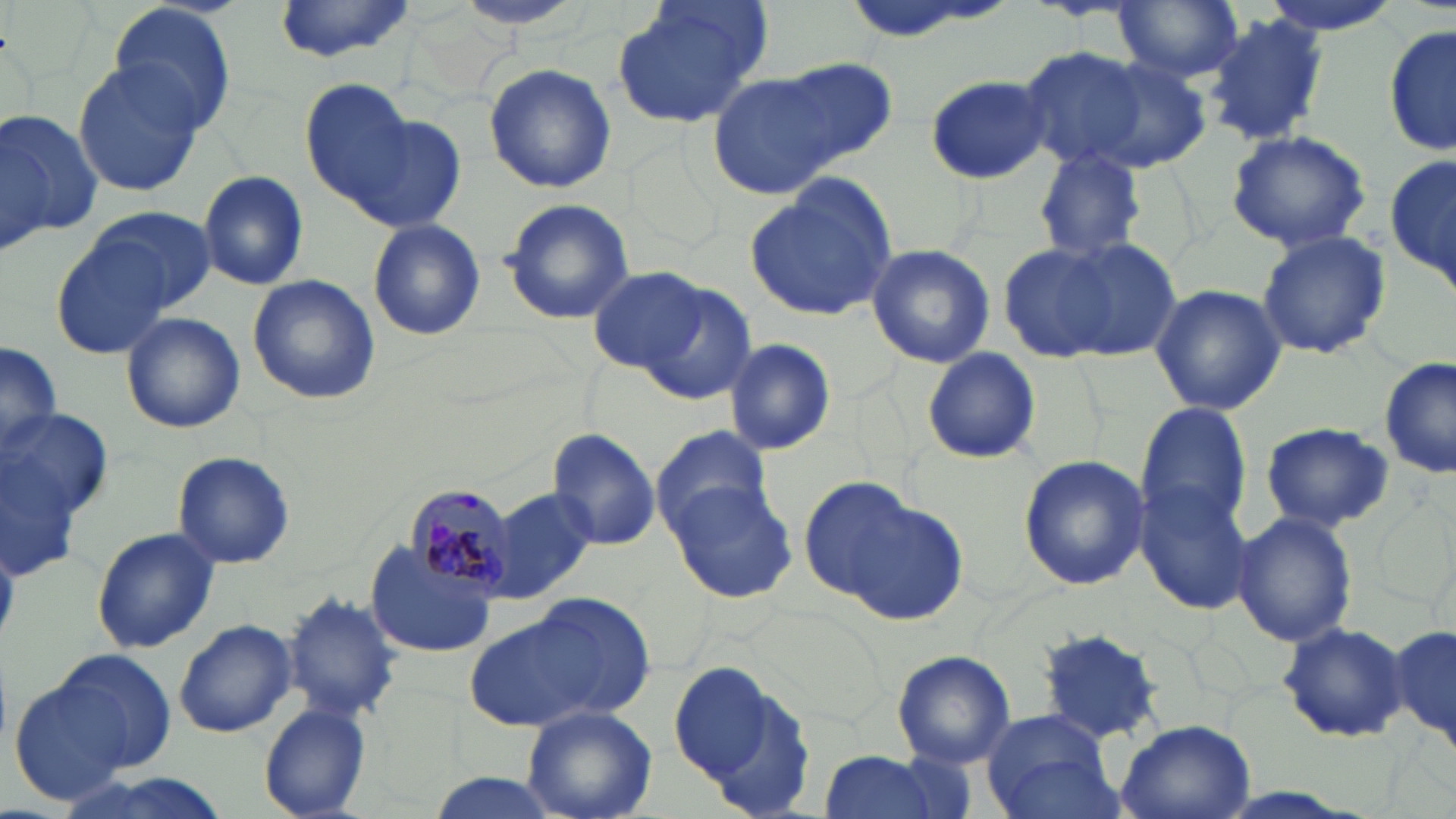

slide-level diagnosis = Plasmodium malariae
stain = May-Grünwald-Giemsa
modality = light microscopy
Plasmodium malariae-infected red blood cell locations = approximate bounding boxes as [x1, y1, x2, y2] in pixels: [400, 483, 522, 603]
preparation = thin blood film
uninfected red blood cell locations = approximate bounding boxes as [x1, y1, x2, y2] in pixels: [272, 0, 417, 62], [459, 0, 591, 30], [609, 0, 771, 130], [1112, 0, 1245, 83], [109, 3, 236, 131], [1203, 15, 1329, 144], [1385, 21, 1456, 162], [1020, 46, 1155, 171], [1063, 54, 1217, 176], [779, 58, 898, 163], [73, 62, 205, 197], [483, 63, 617, 193], [706, 70, 857, 202], [921, 72, 1051, 183], [300, 81, 420, 209], [0, 109, 100, 243], [343, 111, 466, 235], [1226, 129, 1372, 253], [1033, 149, 1151, 267], [1386, 152, 1455, 295], [198, 172, 310, 289], [745, 178, 897, 323], [500, 199, 635, 323], [91, 206, 215, 312], [367, 217, 486, 342], [1254, 230, 1392, 359], [50, 233, 175, 359], [1028, 234, 1185, 363], [866, 243, 995, 368], [589, 266, 706, 373], [247, 275, 380, 405], [639, 278, 755, 404], [1149, 283, 1286, 415], [118, 310, 246, 433], [722, 338, 837, 457], [0, 341, 61, 458], [918, 349, 1042, 466], [1378, 356, 1455, 479], [1134, 402, 1251, 535], [2, 412, 116, 530], [1261, 424, 1395, 532], [651, 427, 775, 531], [548, 428, 661, 553], [170, 450, 297, 570], [1019, 455, 1148, 591], [1138, 479, 1256, 613], [666, 482, 799, 605], [825, 485, 970, 625], [486, 488, 600, 605], [1232, 510, 1359, 649], [90, 528, 220, 653], [365, 540, 497, 661], [283, 588, 402, 723], [525, 591, 656, 722], [465, 612, 605, 731], [173, 618, 297, 736], [1390, 618, 1454, 757], [1278, 619, 1409, 744], [1035, 628, 1166, 743], [25, 649, 179, 796], [668, 650, 817, 815], [891, 650, 1017, 768], [521, 705, 657, 819], [259, 706, 372, 817], [979, 708, 1123, 819], [1116, 718, 1259, 819], [818, 752, 940, 819], [417, 772, 567, 819]
magnification = 1000x
field of view = one of a larger specimen
image size = 1456×819 pixels